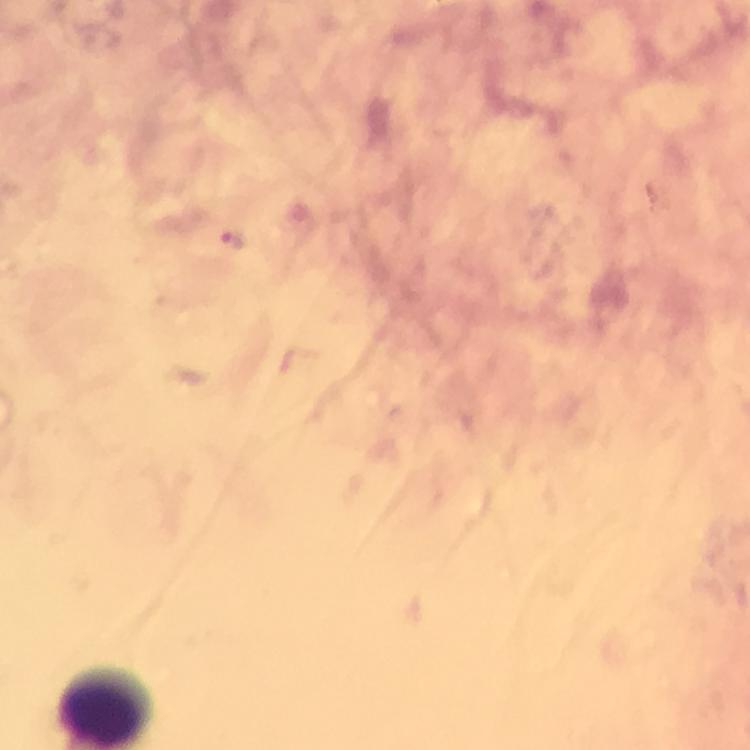

{
  "capture": "smartphone mounted on the microscope",
  "magnification": "100x",
  "stain": "Giemsa",
  "preparation": "thick smear",
  "context": "from a malaria diagnostic workup",
  "immersion_oil": "used",
  "malaria_parasite_locations": "approximate centers as [x, y] in pixels: [233, 238]",
  "cropped_from": "a single field of view",
  "image_size": "750×750 pixels"
}